Report the malaria status of this cell.
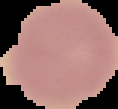
It is uninfected.

From a thin blood smear. The area outside the segmented cell region is set to black. Image is 118×109 pixels.